Describe the morphology of the erythrocytes.
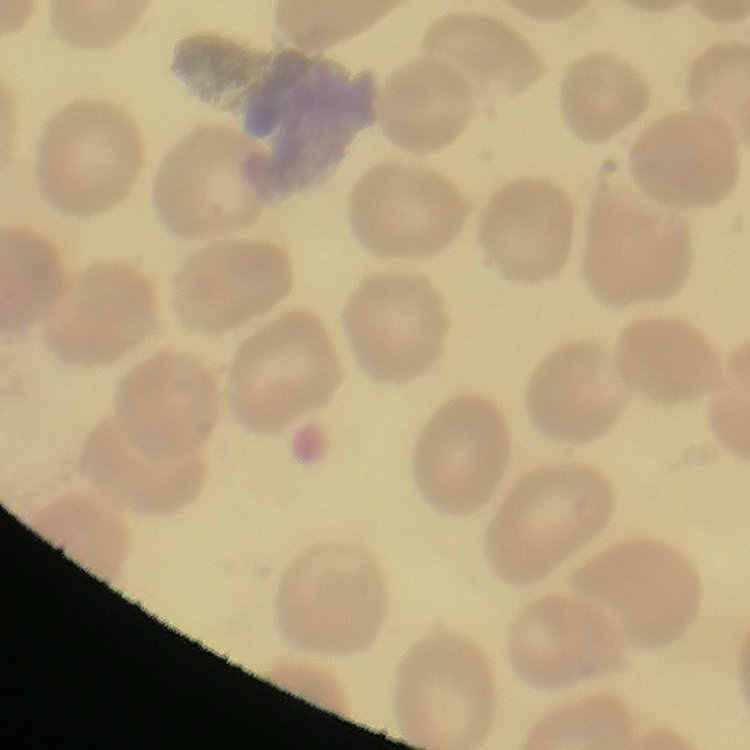

They show no rouleaux formation.

Summary:
  - Stain: Field's or Giemsa
  - Preparation: thin blood smear
  - Image type: one tile cut from a larger photomicrograph